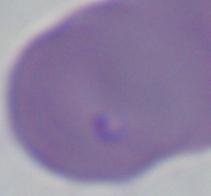
Summary:
  - Modality: photomicrograph
  - Identification: Babesia
  - Magnification: 1000x